State the blood parasite species.
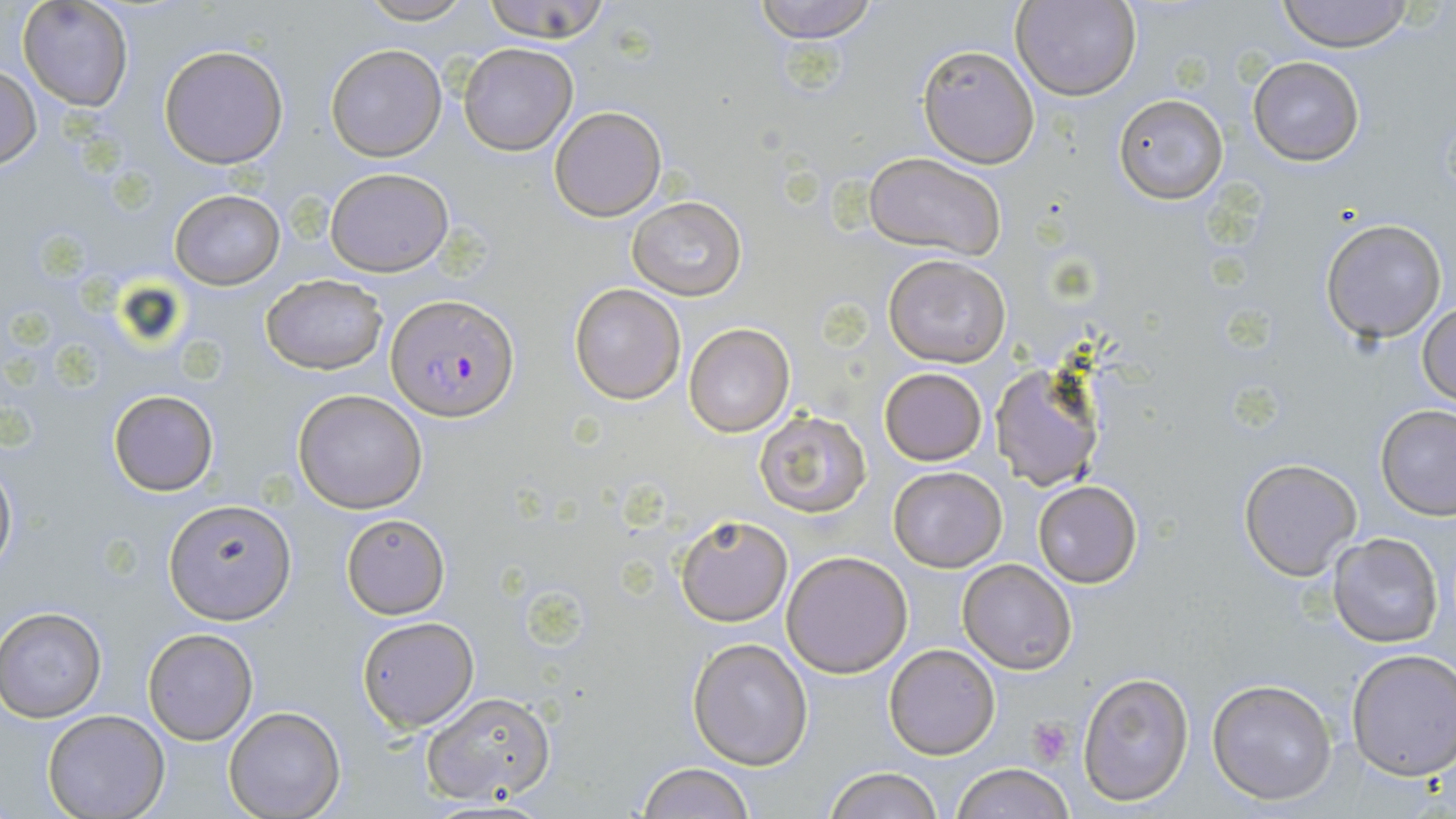

Plasmodium falciparum.

Approximate bounding boxes as (x1, y1, x2, y2) in pixels. Platelet locations: (1028, 717, 1074, 766). Plasmodium falciparum-infected red blood cell locations: (386, 294, 517, 422). Uninfected red blood cell locations: (355, 0, 477, 25), (480, 0, 615, 44), (750, 0, 881, 43), (1014, 0, 1141, 101), (1276, 0, 1414, 51), (18, 1, 134, 112), (158, 43, 289, 169), (457, 43, 578, 155), (326, 44, 445, 161), (918, 45, 1039, 168), (1247, 57, 1364, 165), (0, 64, 41, 170), (1113, 94, 1228, 204), (549, 105, 667, 222), (862, 152, 1006, 260), (324, 167, 453, 276), (169, 189, 285, 290), (627, 196, 745, 301), (1320, 218, 1447, 343), (884, 253, 1012, 368), (260, 274, 387, 376), (568, 283, 686, 405), (1416, 299, 1456, 406), (683, 321, 795, 437), (989, 362, 1106, 491), (879, 367, 987, 465), (294, 389, 428, 514), (108, 390, 218, 496), (1377, 403, 1456, 519), (754, 408, 871, 517), (0, 453, 17, 580), (1239, 457, 1363, 581), (889, 465, 1007, 571), (1032, 480, 1144, 587), (166, 502, 294, 626), (340, 513, 451, 617), (673, 513, 792, 626), (1328, 532, 1444, 648), (781, 551, 913, 677), (957, 558, 1076, 675), (1, 607, 106, 721), (356, 615, 479, 731), (143, 628, 257, 745), (689, 638, 813, 768), (883, 643, 1001, 760), (1346, 648, 1456, 780), (1078, 671, 1195, 806), (1207, 677, 1338, 805), (419, 691, 557, 807), (223, 706, 345, 819), (42, 710, 169, 819), (635, 761, 757, 818), (949, 762, 1075, 819), (823, 767, 945, 819). May-Grünwald-Giemsa stain. Thin blood smear. 1000x magnification. Image is 1456×819 pixels. Optical microscopy. Single field of view.